Locate every blood parasite and identify its species.
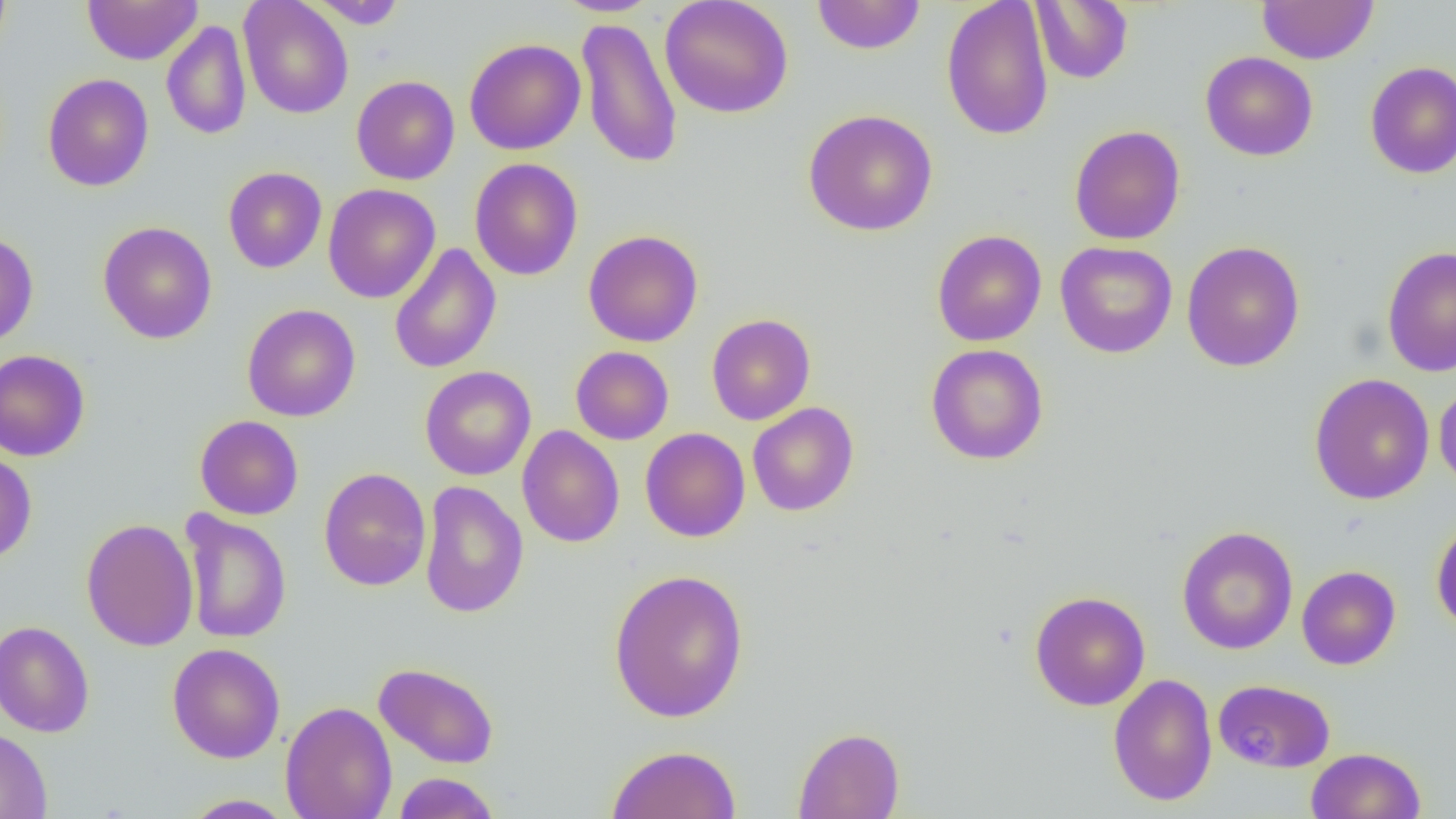

No blood parasites seen.

Summary:
  - Coordinate format: approximate bounding boxes as (x1, y1, x2, y2) in pixels
  - Uninfected red blood cell locations: (0, 0, 12, 63), (82, 0, 203, 65), (238, 0, 354, 119), (552, 0, 663, 17), (660, 0, 794, 118), (811, 0, 926, 55), (941, 0, 1054, 141), (1257, 0, 1378, 64), (307, 1, 408, 29), (1031, 1, 1133, 84), (576, 16, 683, 170), (161, 20, 252, 141), (464, 38, 586, 155), (1199, 51, 1318, 161), (1364, 61, 1456, 179), (42, 73, 154, 192), (351, 75, 460, 185), (803, 109, 938, 236), (1069, 124, 1185, 245), (469, 158, 583, 281), (223, 167, 327, 273), (323, 184, 440, 303), (97, 221, 217, 344), (584, 229, 703, 347), (932, 230, 1047, 347), (0, 232, 38, 348), (1054, 241, 1178, 358), (1181, 241, 1306, 372), (388, 243, 502, 374), (1382, 246, 1456, 377), (242, 303, 360, 422), (706, 313, 816, 425), (925, 343, 1049, 465), (571, 346, 674, 445), (0, 349, 90, 462), (420, 365, 536, 481), (1308, 372, 1435, 505), (1434, 380, 1456, 495), (747, 402, 859, 516), (194, 415, 303, 520), (517, 425, 625, 548), (640, 427, 750, 542), (0, 450, 37, 564), (318, 467, 431, 591), (419, 481, 529, 618), (179, 509, 292, 644), (1431, 516, 1456, 635), (81, 517, 199, 652), (1176, 526, 1299, 655), (1296, 565, 1401, 669), (608, 568, 749, 724), (1029, 590, 1150, 711), (0, 620, 95, 738), (167, 643, 285, 763), (374, 662, 499, 768), (1108, 674, 1218, 806), (1213, 678, 1335, 772), (280, 701, 397, 819), (792, 727, 905, 819), (0, 728, 52, 819), (606, 744, 742, 819), (1306, 747, 1426, 819), (393, 772, 501, 818), (181, 794, 297, 818)
  - Slide-level diagnosis: negative for blood parasites
  - Field of view: one of a larger specimen
  - Preparation: thin blood film
  - Magnification: 1000x
  - Modality: optical microscopy
  - Image size: 1456×819 pixels